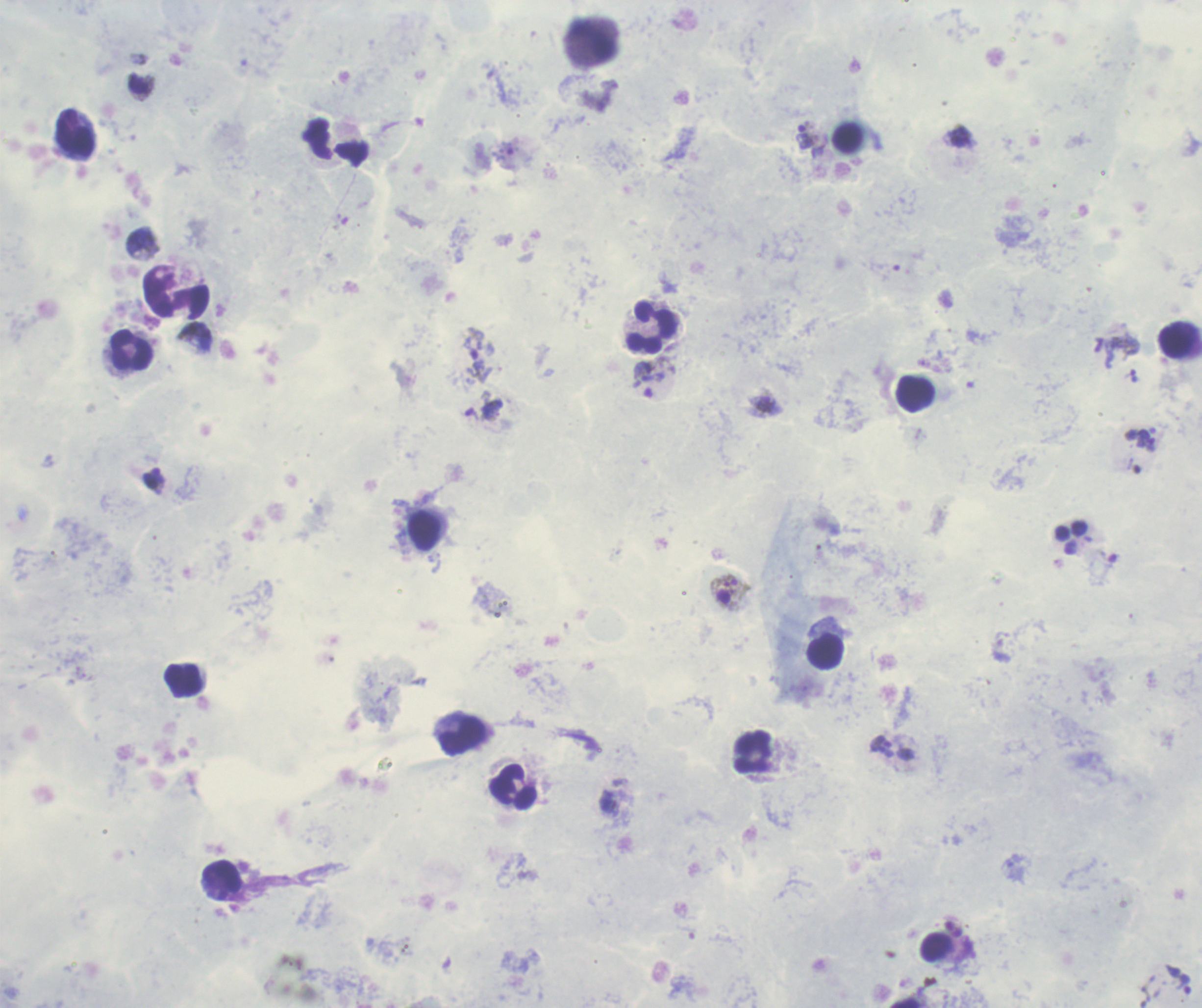
Approximate object centers, in pixels from the top-left corner. Gametocyte locations: (x=729, y=593). Leukocyte locations: (x=593, y=41), (x=75, y=133), (x=336, y=142), (x=653, y=328), (x=1178, y=341), (x=131, y=349), (x=915, y=395), (x=425, y=531), (x=827, y=653), (x=184, y=681), (x=463, y=736), (x=754, y=752), (x=514, y=787), (x=222, y=879), (x=937, y=946). Trophozoite locations: (x=805, y=134), (x=648, y=379), (x=766, y=405), (x=153, y=480), (x=881, y=746), (x=1178, y=979). Life-cycle stages observed: trophozoite, gametocyte. Single field of view. Coloration quality: good. Image is 1202×1008 pixels. Romanowsky stain. Result: Plasmodium parasites detected. Background quality: poor. Previously used in a real diagnosis. Captured at 100x magnification. Thick smear of blood.